Classify this cell by malaria status.
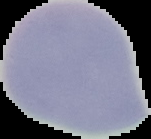
It is uninfected.

Summary:
  - Image type: segmented cell region on a black background
  - Preparation: thin blood smear
  - Image size: 151×139 pixels